Classify this cell by malaria status.
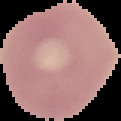

It is uninfected.

preparation = thin blood film
image size = 121×121 pixels
image type = cell region segmented out of the field of view; surrounding area masked to black